Report the malaria status of this cell.
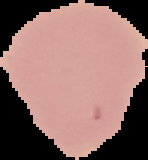
It is uninfected.

preparation: thin blood film
image_size: 148×160 pixels
image_type: cell region segmented out of the field of view; surrounding area masked to black